Describe the morphology of the erythrocytes.
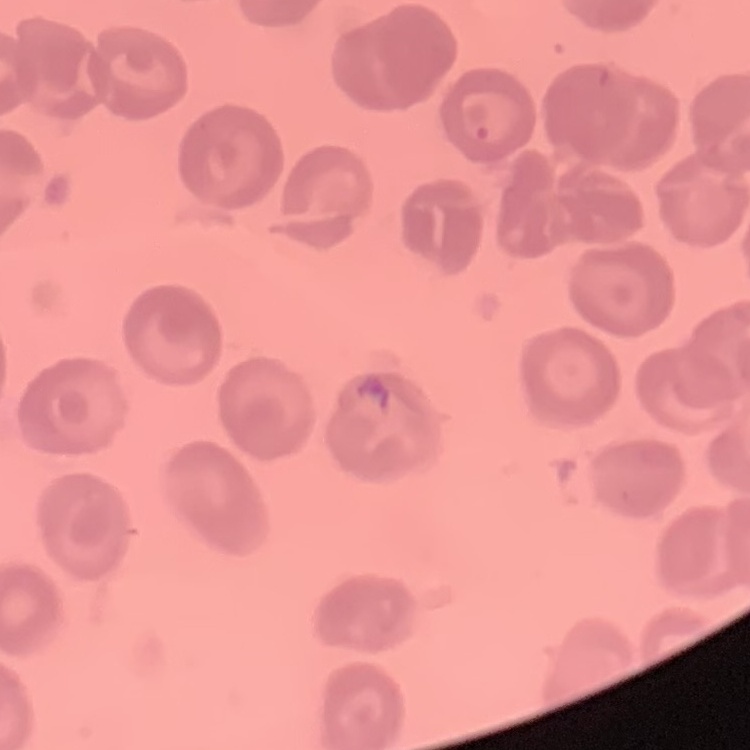

They show no rouleaux formation.

One tile cut from a larger photomicrograph. Thin peripheral smear. Field's or Giemsa stain.